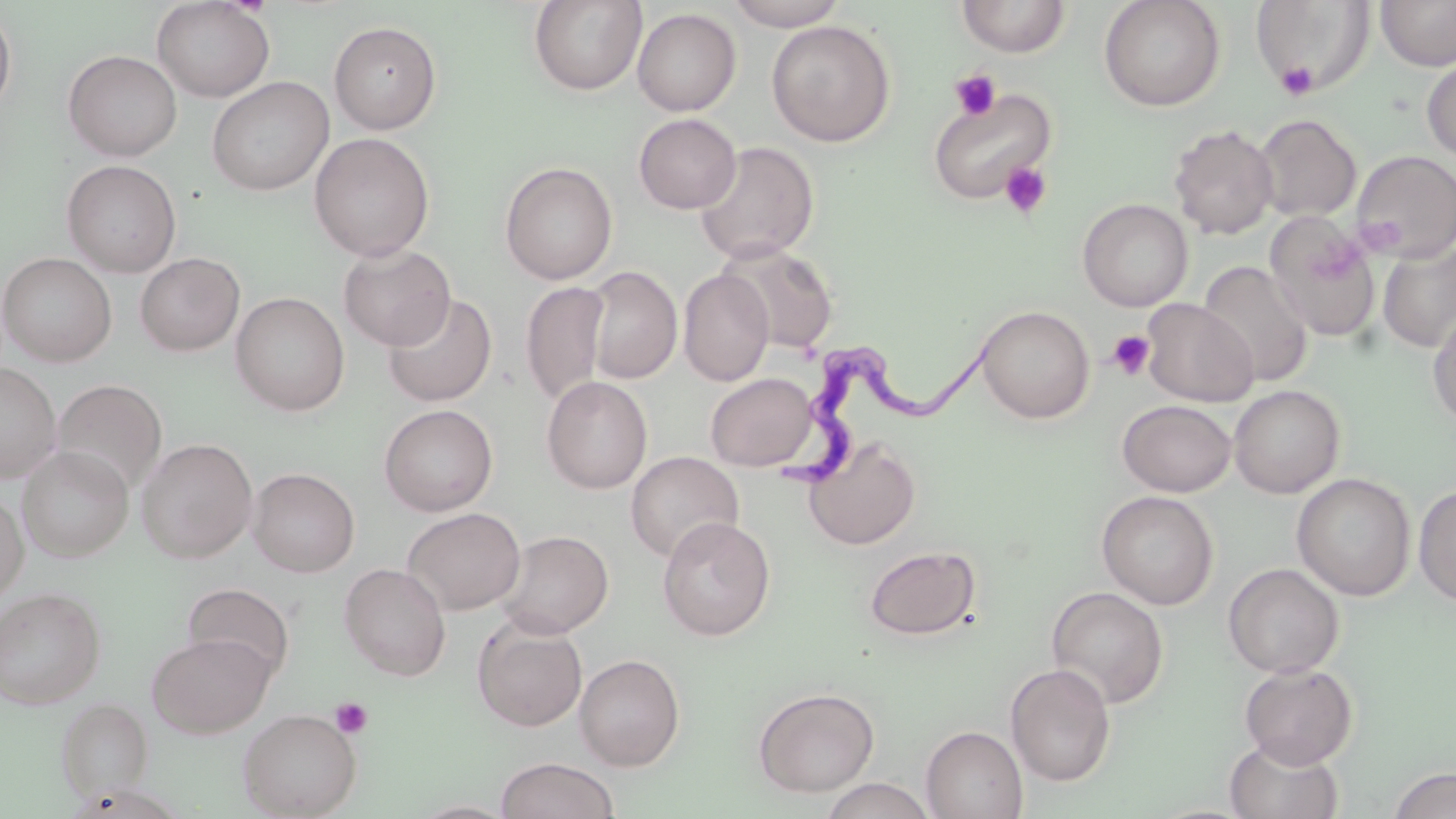
Summary:
  - Coordinate format: approximate bounding boxes as (x1, y1, x2, y2) in pixels
  - Uninfected red blood cell locations: (151, 0, 275, 102), (528, 0, 647, 96), (724, 0, 849, 30), (955, 0, 1071, 57), (1098, 0, 1225, 112), (1252, 0, 1374, 95), (1375, 0, 1456, 70), (0, 5, 17, 121), (632, 8, 742, 116), (328, 20, 442, 134), (766, 20, 896, 147), (63, 49, 182, 161), (1421, 56, 1456, 163), (206, 76, 334, 196), (927, 89, 1057, 205), (633, 113, 742, 214), (1254, 114, 1361, 222), (1168, 124, 1278, 239), (309, 132, 435, 261), (694, 141, 819, 264), (1351, 150, 1455, 262), (61, 159, 182, 277), (499, 161, 618, 284), (1077, 198, 1194, 311), (1265, 214, 1382, 341), (718, 243, 839, 354), (1378, 243, 1456, 353), (338, 244, 456, 350), (0, 252, 117, 367), (135, 252, 245, 356), (1199, 260, 1313, 388), (584, 265, 681, 384), (678, 269, 774, 386), (519, 281, 611, 407), (230, 291, 350, 416), (381, 292, 498, 407), (1140, 298, 1258, 407), (976, 305, 1095, 424), (1428, 308, 1456, 428), (0, 362, 61, 483), (704, 373, 819, 471), (541, 375, 653, 494), (52, 379, 167, 497), (1228, 384, 1345, 498), (1117, 400, 1236, 497), (379, 404, 498, 516), (136, 437, 258, 563), (804, 438, 921, 550), (17, 444, 134, 562), (625, 451, 744, 562), (247, 467, 360, 577), (1292, 472, 1416, 601), (1414, 484, 1456, 606), (1096, 490, 1219, 609), (0, 491, 28, 606), (402, 507, 525, 615), (657, 515, 776, 640), (495, 529, 614, 638), (864, 545, 981, 640), (338, 562, 452, 681), (1223, 563, 1344, 678), (181, 582, 295, 684), (0, 586, 106, 709), (1046, 586, 1168, 709), (472, 616, 588, 732), (147, 632, 274, 738), (574, 653, 685, 771), (1239, 661, 1358, 767), (1005, 662, 1116, 786), (753, 686, 880, 797), (56, 696, 153, 802), (237, 709, 362, 818), (921, 726, 1028, 819), (1225, 737, 1344, 819), (496, 757, 619, 819), (1387, 767, 1455, 818), (818, 777, 937, 819), (410, 799, 519, 818)
  - Trypanosoma brucei locations: (783, 328, 1008, 497)
  - Platelet locations: (1276, 61, 1319, 101), (948, 69, 1001, 120), (999, 160, 1053, 220), (1107, 329, 1156, 381), (330, 697, 373, 739)
  - Slide-level diagnosis: Trypanosoma brucei
  - Image size: 1456×819 pixels
  - Field of view: one of a larger specimen
  - Stain: May-Grünwald-Giemsa
  - Magnification: 1000x
  - Modality: light microscopy
  - Preparation: thin blood smear